Identify the cell.
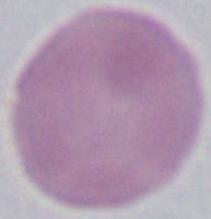

This is an erythrocyte.

Summary:
  - Magnification: 1000x
  - Modality: photomicrograph